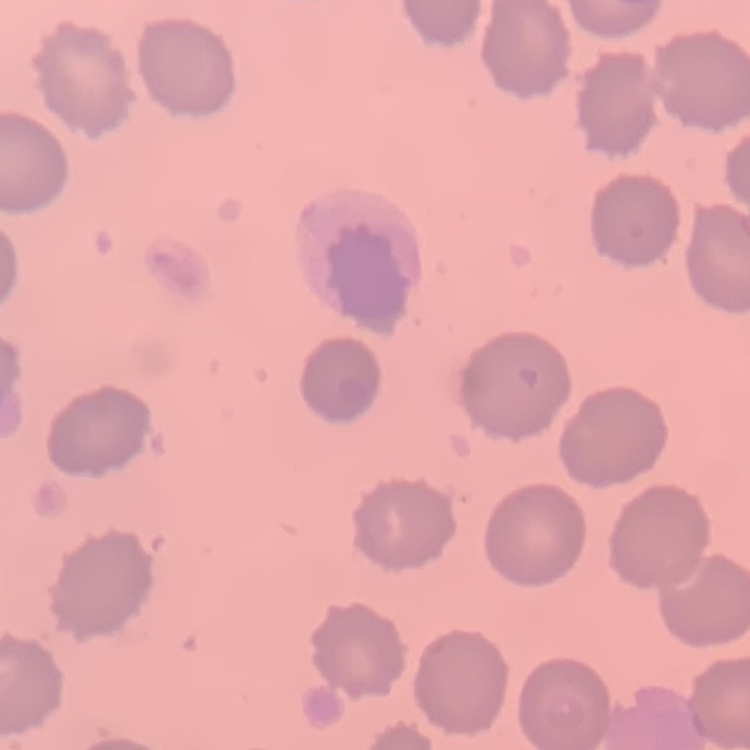
Summary:
  - Erythrocyte morphology: no rouleaux formation
  - Preparation: thin blood smear
  - Stain: Field's or Giemsa
  - Image type: one tile cut from a larger photomicrograph